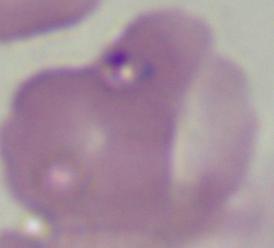
modality: photomicrograph
identification: Babesia
magnification: 1000x